Report the malaria status of this cell.
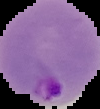

Parasitized.

Summary:
  - Preparation: thin blood smear
  - Image type: cell region segmented out of the field of view; surrounding area masked to black
  - Image size: 100×109 pixels